Assess the morphology of the red blood cells.
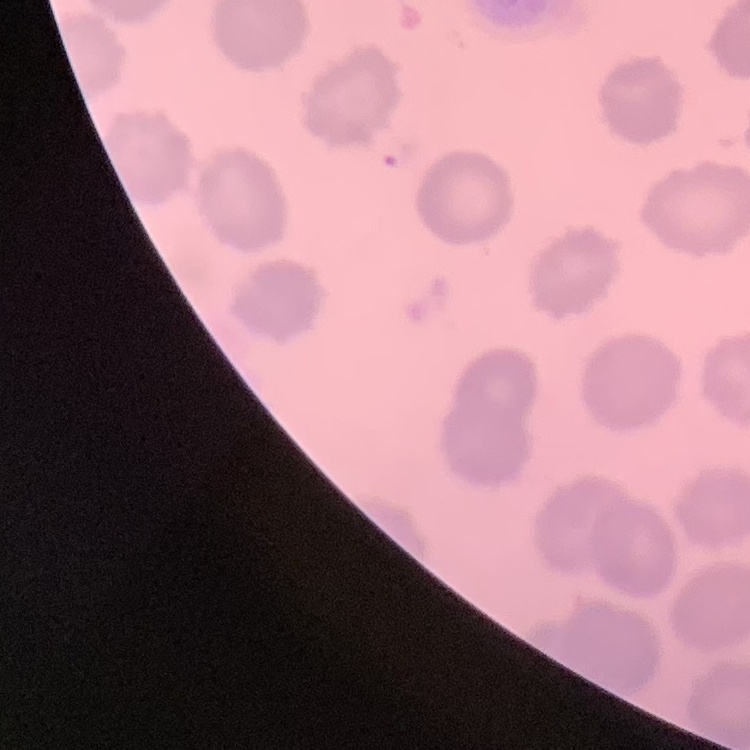
No rouleaux formation.

preparation = thin blood film
stain = Field's or Giemsa
image type = square crop of a larger photomicrograph